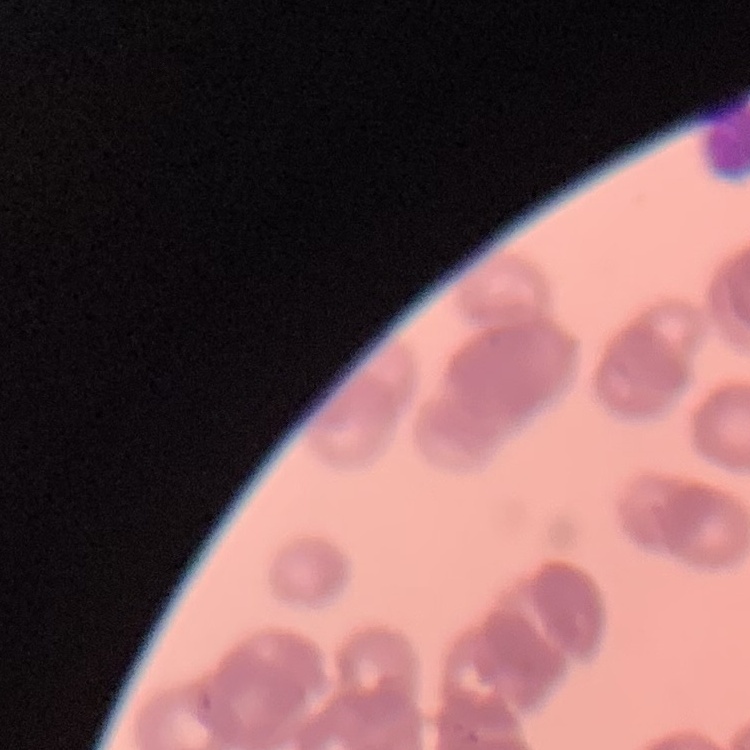
red_blood_cell_morphology: rouleaux formation
preparation: thin peripheral smear
image_type: square crop of a larger photomicrograph
stain: Field's or Giemsa